Locate every blood parasite and identify its species.
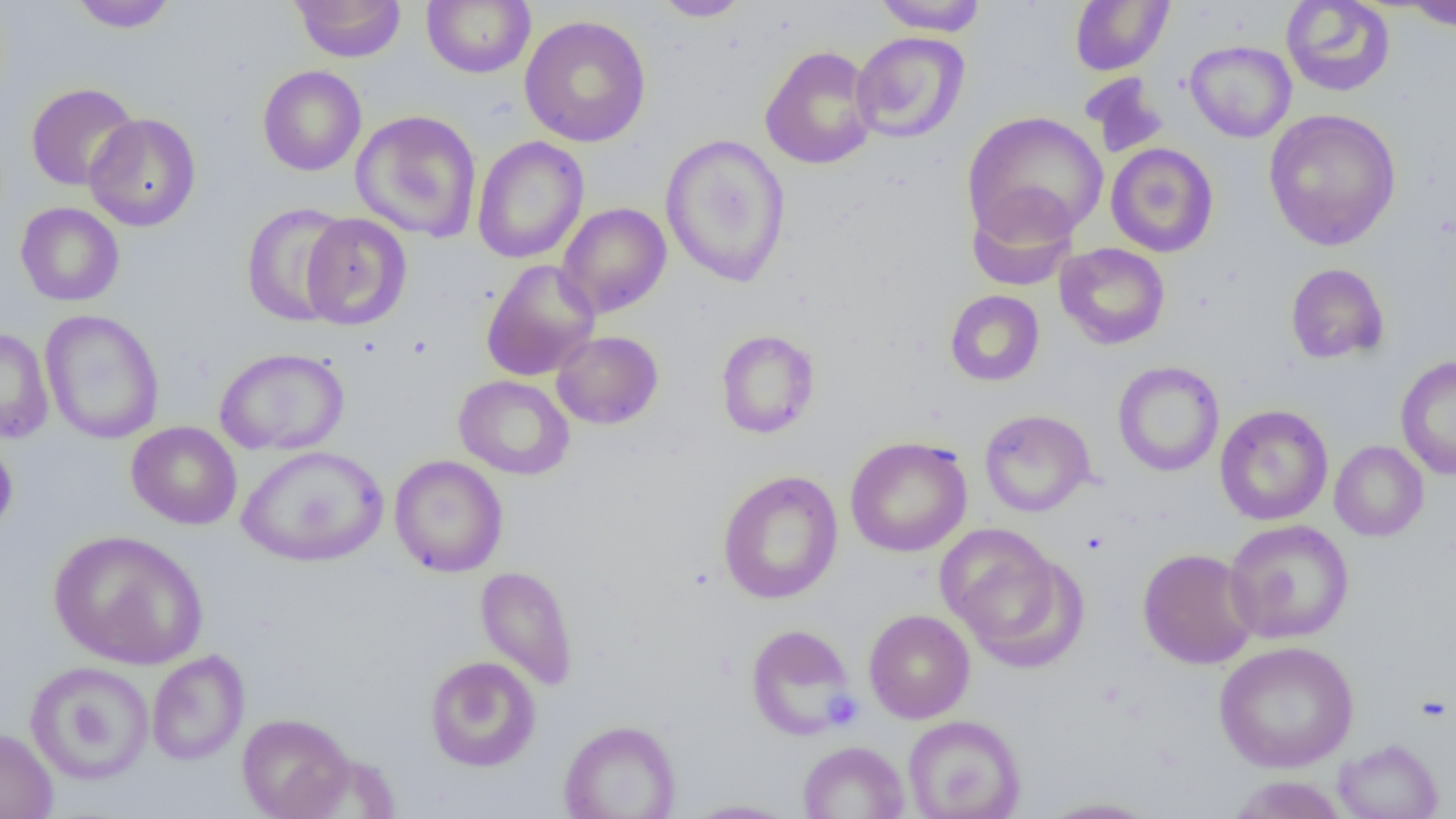

No blood parasites observed.

slide_level_diagnosis: no evidence of blood parasites
image_size: 1456×819 pixels
platelet_locations: 'approximate bounding boxes as named x1/y1/x2/y2 corners in pixels: (x1=821, y1=690, x2=863, y2=730)'
preparation: thin blood film
field_of_view: single
modality: light microscopy
magnification: 1000x
uninfected_red_blood_cell_locations: 'approximate bounding boxes as named x1/y1/x2/y2 corners in pixels: (x1=68, y1=0, x2=178, y2=32), (x1=422, y1=0, x2=536, y2=78), (x1=873, y1=0, x2=988, y2=35), (x1=1070, y1=0, x2=1173, y2=75), (x1=1280, y1=0, x2=1396, y2=97), (x1=291, y1=1, x2=406, y2=62), (x1=651, y1=1, x2=753, y2=21), (x1=1398, y1=1, x2=1456, y2=32), (x1=519, y1=14, x2=651, y2=147), (x1=851, y1=31, x2=970, y2=143), (x1=1185, y1=40, x2=1297, y2=142), (x1=760, y1=45, x2=878, y2=170), (x1=257, y1=65, x2=367, y2=176), (x1=1081, y1=73, x2=1169, y2=158), (x1=26, y1=83, x2=140, y2=191), (x1=1263, y1=107, x2=1402, y2=250), (x1=351, y1=110, x2=482, y2=242), (x1=962, y1=111, x2=1108, y2=244), (x1=84, y1=113, x2=201, y2=232), (x1=660, y1=133, x2=792, y2=288), (x1=472, y1=136, x2=589, y2=265), (x1=1106, y1=142, x2=1219, y2=258), (x1=966, y1=188, x2=1080, y2=291), (x1=240, y1=201, x2=354, y2=327), (x1=15, y1=202, x2=124, y2=306), (x1=557, y1=202, x2=672, y2=318), (x1=300, y1=213, x2=412, y2=331), (x1=1055, y1=242, x2=1170, y2=349), (x1=481, y1=260, x2=599, y2=381), (x1=1286, y1=263, x2=1389, y2=364), (x1=944, y1=290, x2=1045, y2=386), (x1=40, y1=309, x2=164, y2=444), (x1=0, y1=327, x2=54, y2=444), (x1=715, y1=329, x2=820, y2=439), (x1=552, y1=331, x2=663, y2=430), (x1=214, y1=347, x2=350, y2=456), (x1=1395, y1=355, x2=1456, y2=479), (x1=1112, y1=360, x2=1225, y2=476), (x1=453, y1=375, x2=575, y2=480), (x1=1215, y1=404, x2=1333, y2=525), (x1=978, y1=409, x2=1095, y2=517), (x1=126, y1=421, x2=242, y2=530), (x1=0, y1=433, x2=18, y2=539), (x1=845, y1=436, x2=972, y2=557), (x1=1329, y1=440, x2=1429, y2=541), (x1=237, y1=445, x2=389, y2=568), (x1=389, y1=455, x2=508, y2=577), (x1=717, y1=470, x2=844, y2=604), (x1=1223, y1=519, x2=1354, y2=644), (x1=938, y1=525, x2=1082, y2=667), (x1=48, y1=529, x2=209, y2=669), (x1=1137, y1=548, x2=1258, y2=669), (x1=475, y1=565, x2=579, y2=690), (x1=863, y1=609, x2=975, y2=724), (x1=745, y1=623, x2=857, y2=740), (x1=1214, y1=640, x2=1360, y2=773), (x1=147, y1=649, x2=249, y2=765), (x1=425, y1=655, x2=541, y2=772), (x1=25, y1=660, x2=155, y2=786), (x1=237, y1=712, x2=356, y2=819), (x1=902, y1=715, x2=1026, y2=819), (x1=558, y1=719, x2=681, y2=819), (x1=0, y1=726, x2=58, y2=819), (x1=1334, y1=738, x2=1443, y2=819), (x1=798, y1=741, x2=910, y2=819), (x1=1226, y1=775, x2=1349, y2=819), (x1=1035, y1=796, x2=1164, y2=818), (x1=680, y1=799, x2=800, y2=818)'